Assess this cell for malaria.
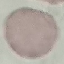
Uninfected.

Summary:
  - Stain: Giemsa
  - Preparation: thin blood film
  - Capture: smartphone camera at the microscope eyepiece
  - Image type: cell patch, automatically extracted from a larger field of view and resized to 64 × 64 pixels